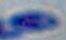
Summary:
  - Identification: Toxoplasma gondii
  - Magnification: 1000x
  - Modality: photomicrograph